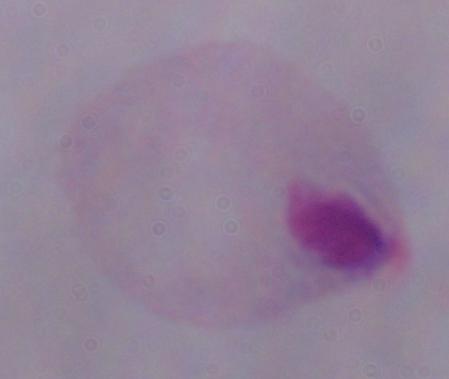

Captured at 1000x magnification. A trichomonad is shown. Photomicrograph.